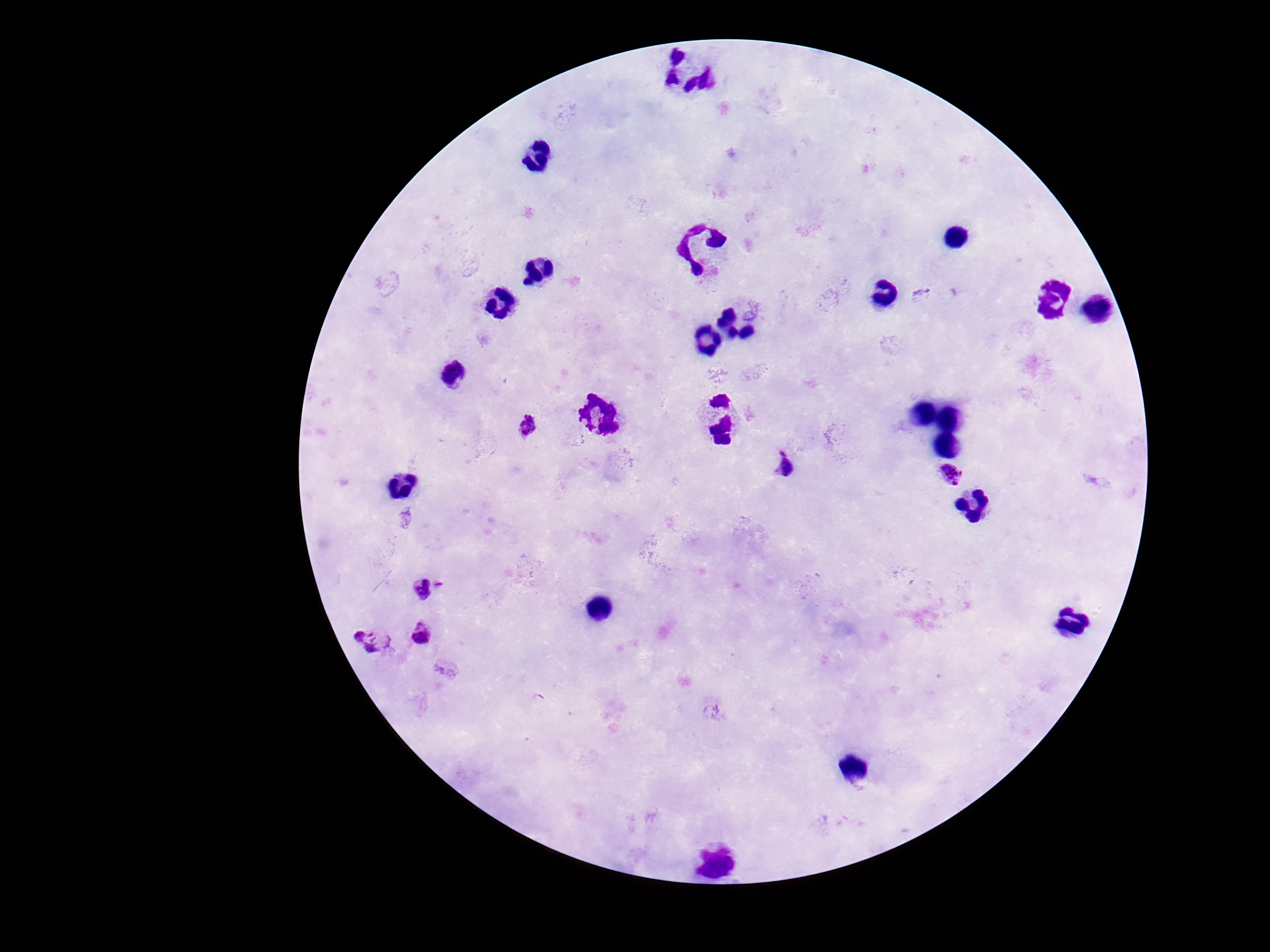

Approximate object centers, in pixels from the top-left corner. Plasmodium parasite locations: (x=923, y=293), (x=527, y=427), (x=783, y=465), (x=950, y=474), (x=440, y=585), (x=421, y=589), (x=421, y=633), (x=373, y=639). Single field of view. 100x magnification. Giemsa-stained preparation. Patient malaria status: positive. Photographed through the microscope eyepiece with a smartphone camera. Image is 1270×952 pixels. Thick blood film.